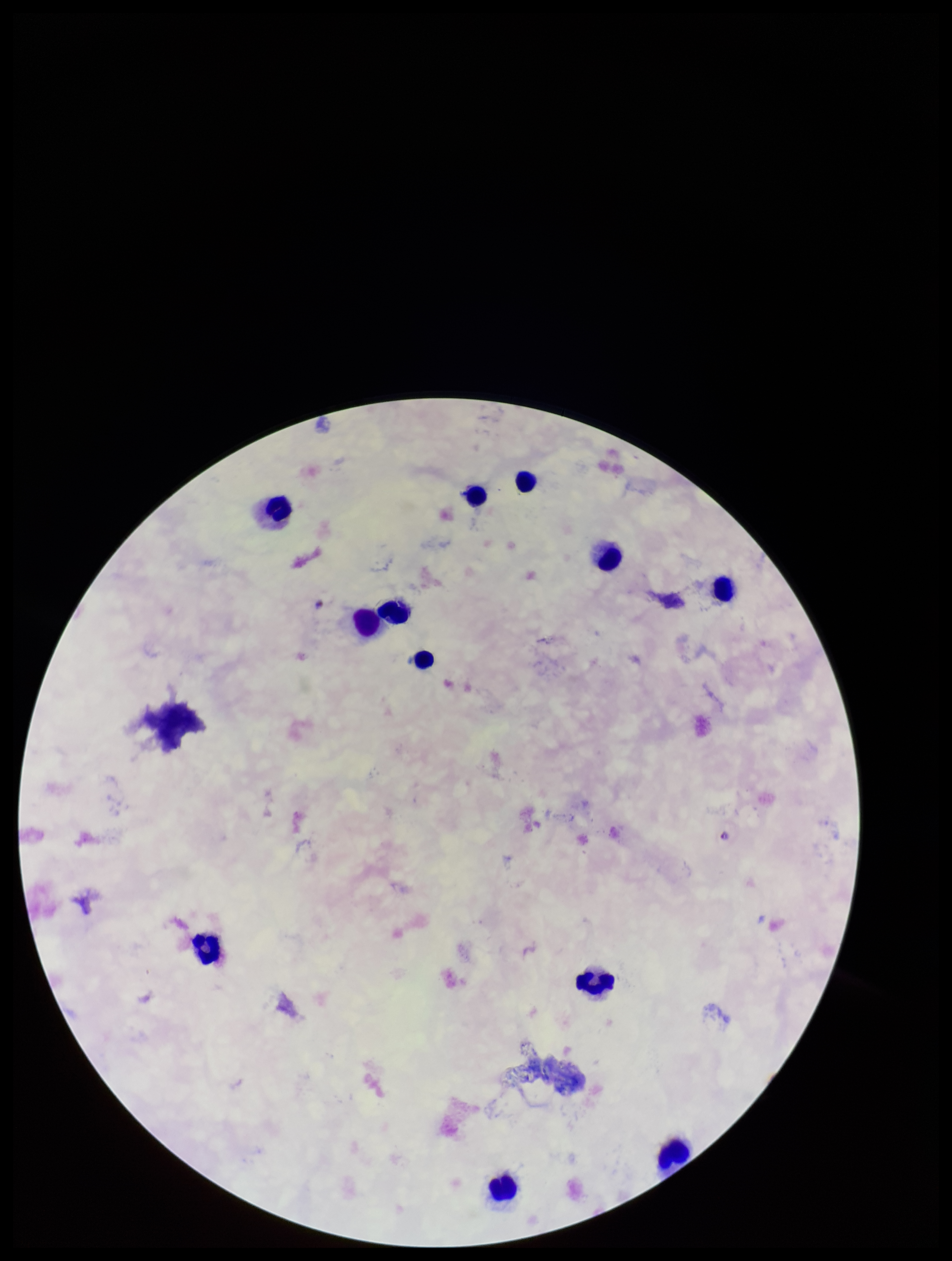
Plasmodium parasites = identified
stain = Giemsa
patient malaria status = infected
capture = smartphone photograph through the microscope eyepiece
image size = 952×1261 pixels
species reported for this patient = Plasmodium falciparum
leukocyte count = 12
parasite count = 1
field of view = one from this slide
preparation = thick blood smear